Give the preparation type.
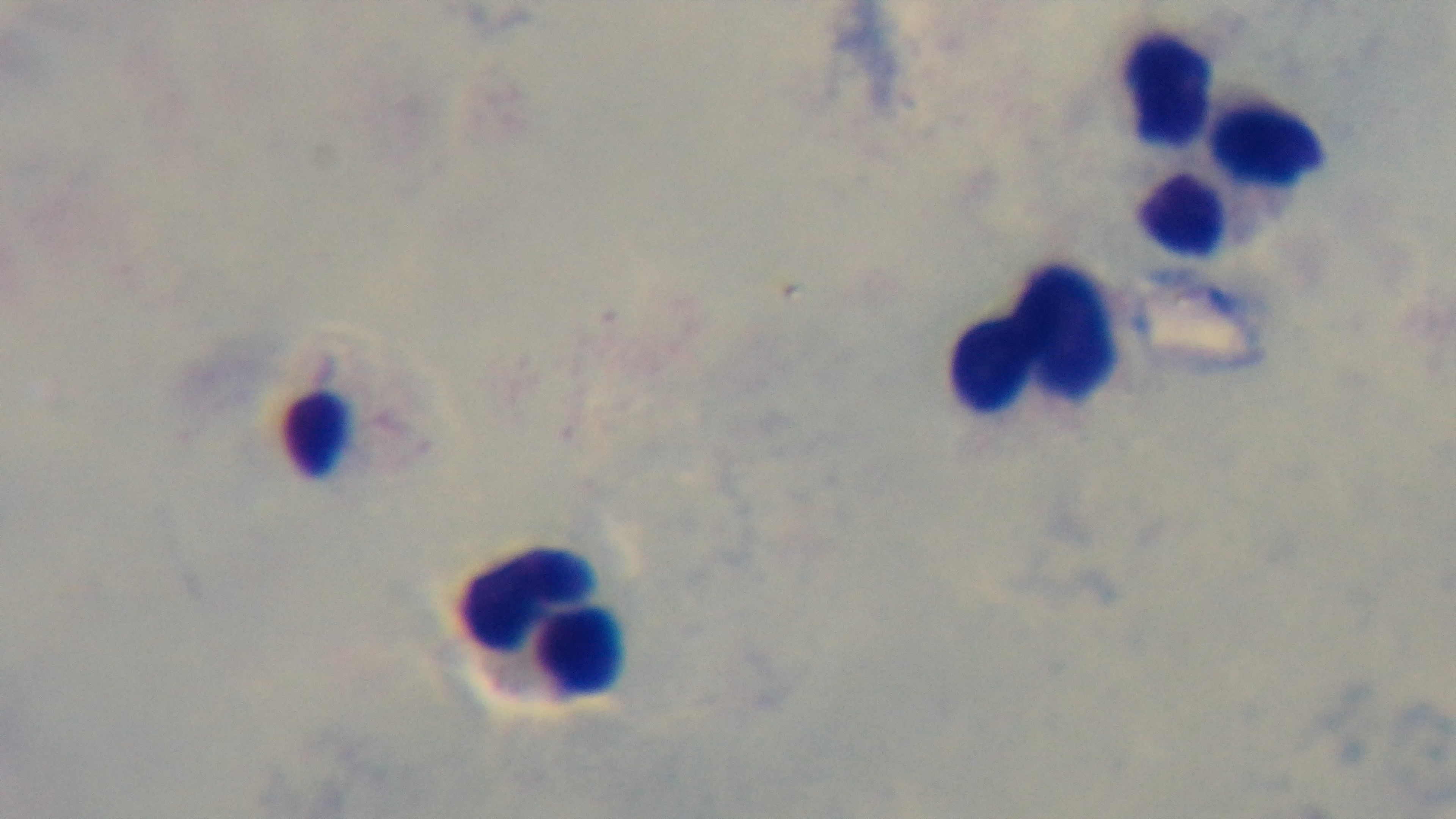
A thick smear.

objective = 100x oil immersion
field of view = one from the slide
malaria status = uninfected
stain = Giemsa
capture = mounted 4K digital camera
modality = light microscopy